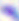
Summary:
  - Modality: micrograph
  - Identification: Toxoplasma gondii
  - Magnification: 400x